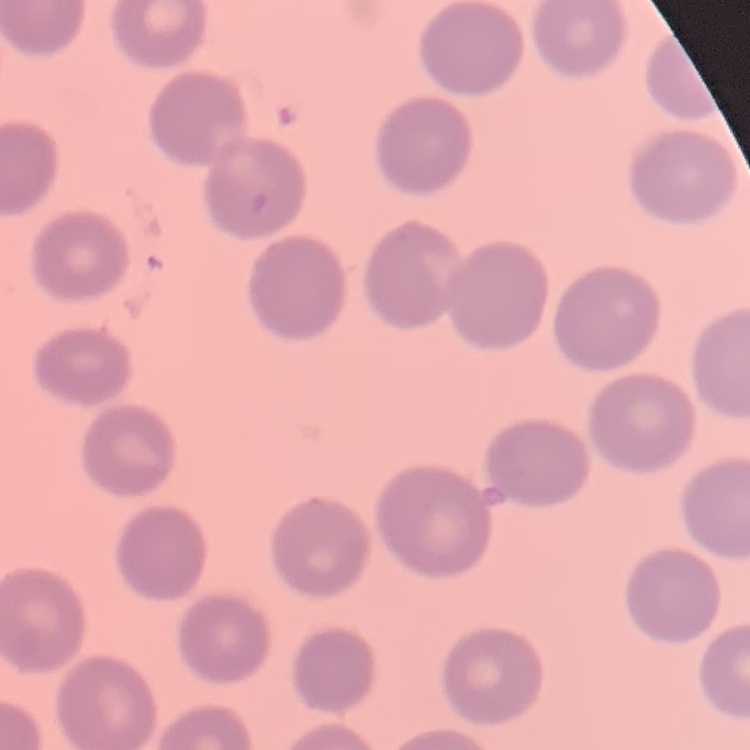

Summary:
  - Erythrocyte morphology: no rouleaux formation
  - Preparation: thin blood film
  - Image type: square crop of a larger photomicrograph
  - Stain: Field's or Giemsa